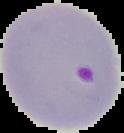

Summary:
  - Malaria status: parasitized
  - Image type: cell region segmented out of the field of view; surrounding area masked to black
  - Preparation: thin blood smear
  - Image size: 124×133 pixels